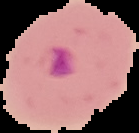

Image is 139×133 pixels. From a thin blood film. Malaria status: parasitized. The area outside the segmented cell region is set to black.